Assess the morphology of the red blood cells.
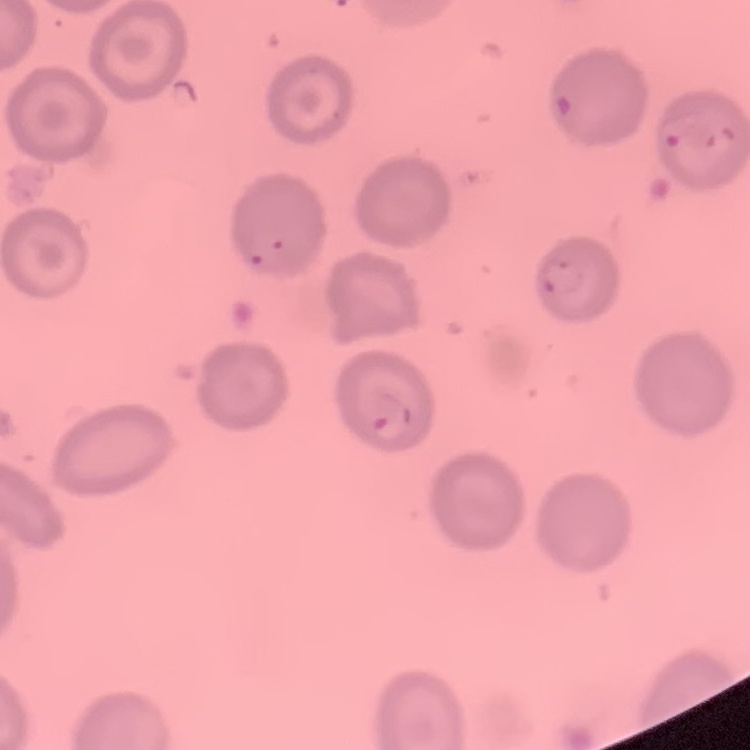

They show no rouleaux formation.

{
  "preparation": "thin blood smear",
  "image_type": "square crop of a larger photomicrograph",
  "stain": "Field's or Giemsa"
}